Report the malaria status of this cell.
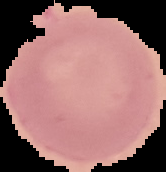

It is uninfected.

preparation = thin blood film
image size = 166×172 pixels
image type = cell region segmented out of the field of view; surrounding area masked to black